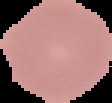
image size = 112×103 pixels
result = negative for Plasmodium parasites
image type = segmented cell region with the area outside set to black
preparation = thin blood smear